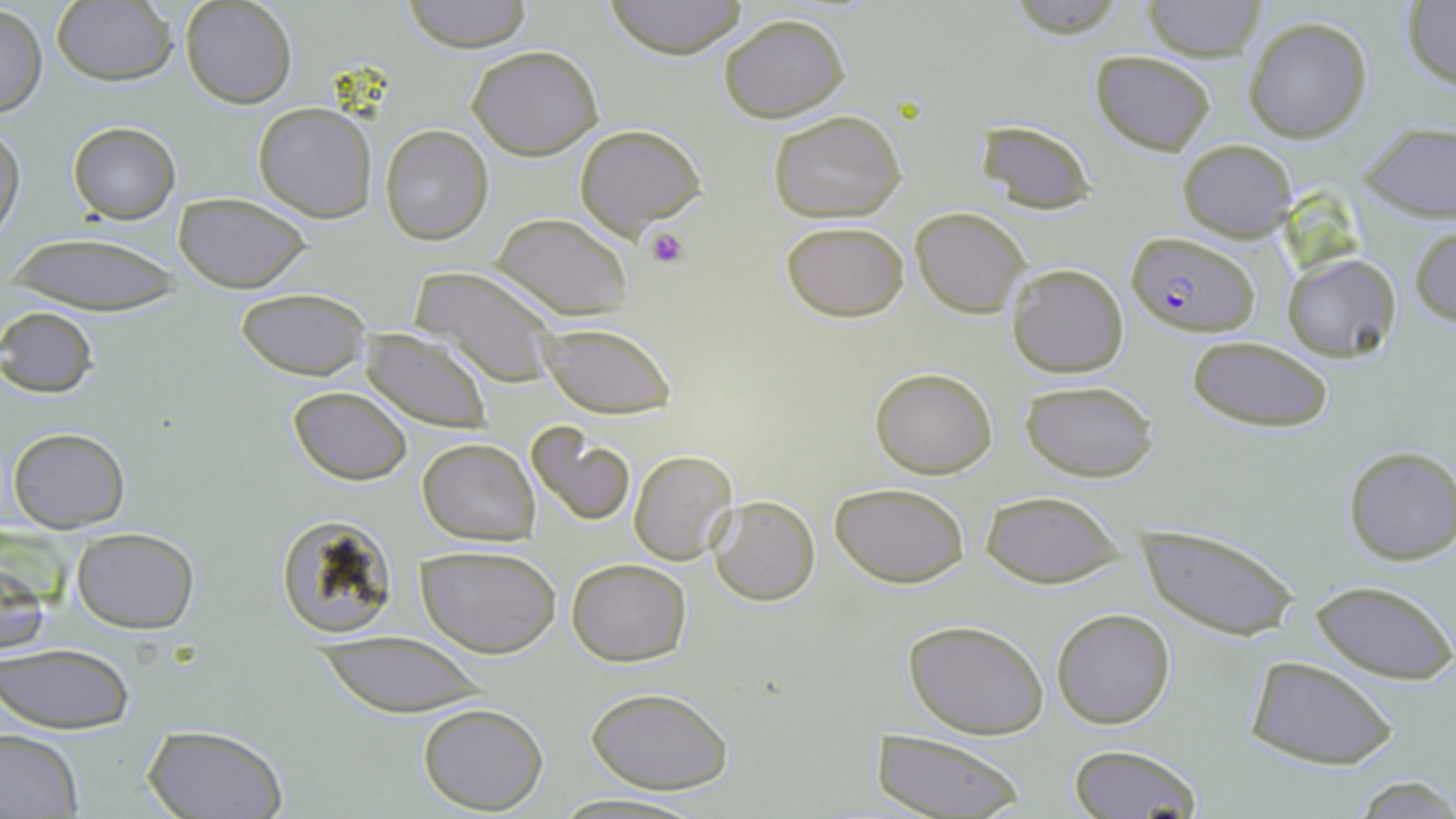
Approximate bounding boxes as named x1/y1/x2/y2 corners in pixels. Uninfected red blood cell locations: (x1=402, y1=0, x2=534, y2=52), (x1=604, y1=0, x2=750, y2=58), (x1=1002, y1=0, x2=1131, y2=38), (x1=52, y1=1, x2=179, y2=86), (x1=180, y1=1, x2=299, y2=108), (x1=1144, y1=1, x2=1265, y2=61), (x1=1402, y1=1, x2=1456, y2=91), (x1=1, y1=3, x2=45, y2=120), (x1=718, y1=13, x2=850, y2=121), (x1=1243, y1=16, x2=1372, y2=141), (x1=466, y1=44, x2=605, y2=162), (x1=1090, y1=50, x2=1216, y2=155), (x1=254, y1=103, x2=378, y2=222), (x1=768, y1=109, x2=908, y2=224), (x1=973, y1=121, x2=1097, y2=214), (x1=68, y1=122, x2=180, y2=224), (x1=0, y1=123, x2=25, y2=241), (x1=576, y1=124, x2=706, y2=239), (x1=1359, y1=124, x2=1455, y2=223), (x1=380, y1=125, x2=493, y2=246), (x1=1177, y1=138, x2=1297, y2=240), (x1=174, y1=192, x2=309, y2=293), (x1=912, y1=207, x2=1028, y2=316), (x1=494, y1=213, x2=632, y2=320), (x1=780, y1=219, x2=910, y2=322), (x1=1410, y1=222, x2=1456, y2=326), (x1=1, y1=233, x2=185, y2=312), (x1=1282, y1=253, x2=1402, y2=362), (x1=1005, y1=263, x2=1129, y2=378), (x1=412, y1=267, x2=561, y2=386), (x1=234, y1=287, x2=370, y2=381), (x1=0, y1=307, x2=99, y2=398), (x1=537, y1=322, x2=677, y2=418), (x1=359, y1=328, x2=492, y2=433), (x1=1187, y1=335, x2=1334, y2=433), (x1=870, y1=367, x2=997, y2=478), (x1=1021, y1=380, x2=1158, y2=482), (x1=287, y1=386, x2=412, y2=484), (x1=525, y1=421, x2=636, y2=526), (x1=8, y1=426, x2=130, y2=532), (x1=418, y1=437, x2=539, y2=546), (x1=1342, y1=445, x2=1456, y2=566), (x1=628, y1=450, x2=736, y2=564), (x1=829, y1=480, x2=972, y2=586), (x1=981, y1=489, x2=1125, y2=589), (x1=709, y1=496, x2=820, y2=606), (x1=276, y1=515, x2=400, y2=640), (x1=1142, y1=525, x2=1300, y2=642), (x1=72, y1=528, x2=199, y2=636), (x1=419, y1=545, x2=561, y2=658), (x1=0, y1=555, x2=50, y2=663), (x1=567, y1=558, x2=691, y2=665), (x1=1310, y1=579, x2=1455, y2=684), (x1=1052, y1=608, x2=1177, y2=730), (x1=903, y1=618, x2=1049, y2=739), (x1=309, y1=634, x2=492, y2=716), (x1=1, y1=642, x2=135, y2=736), (x1=4, y1=644, x2=105, y2=817), (x1=1247, y1=657, x2=1397, y2=769), (x1=585, y1=686, x2=734, y2=795), (x1=418, y1=702, x2=549, y2=814), (x1=139, y1=724, x2=290, y2=819), (x1=870, y1=729, x2=1025, y2=818), (x1=0, y1=730, x2=82, y2=818), (x1=1066, y1=743, x2=1204, y2=819), (x1=1348, y1=775, x2=1456, y2=816), (x1=547, y1=793, x2=706, y2=819). Plasmodium falciparum-infected red blood cell locations: (x1=1127, y1=232, x2=1261, y2=338). Platelet locations: (x1=648, y1=226, x2=689, y2=269). Slide-level diagnosis: Plasmodium falciparum. Optical microscopy. 1000x magnification. Image is 1456×819 pixels. Thin blood smear. Single field of view. May-Grünwald-Giemsa-stained preparation.